Find each parasitized red blood cell.
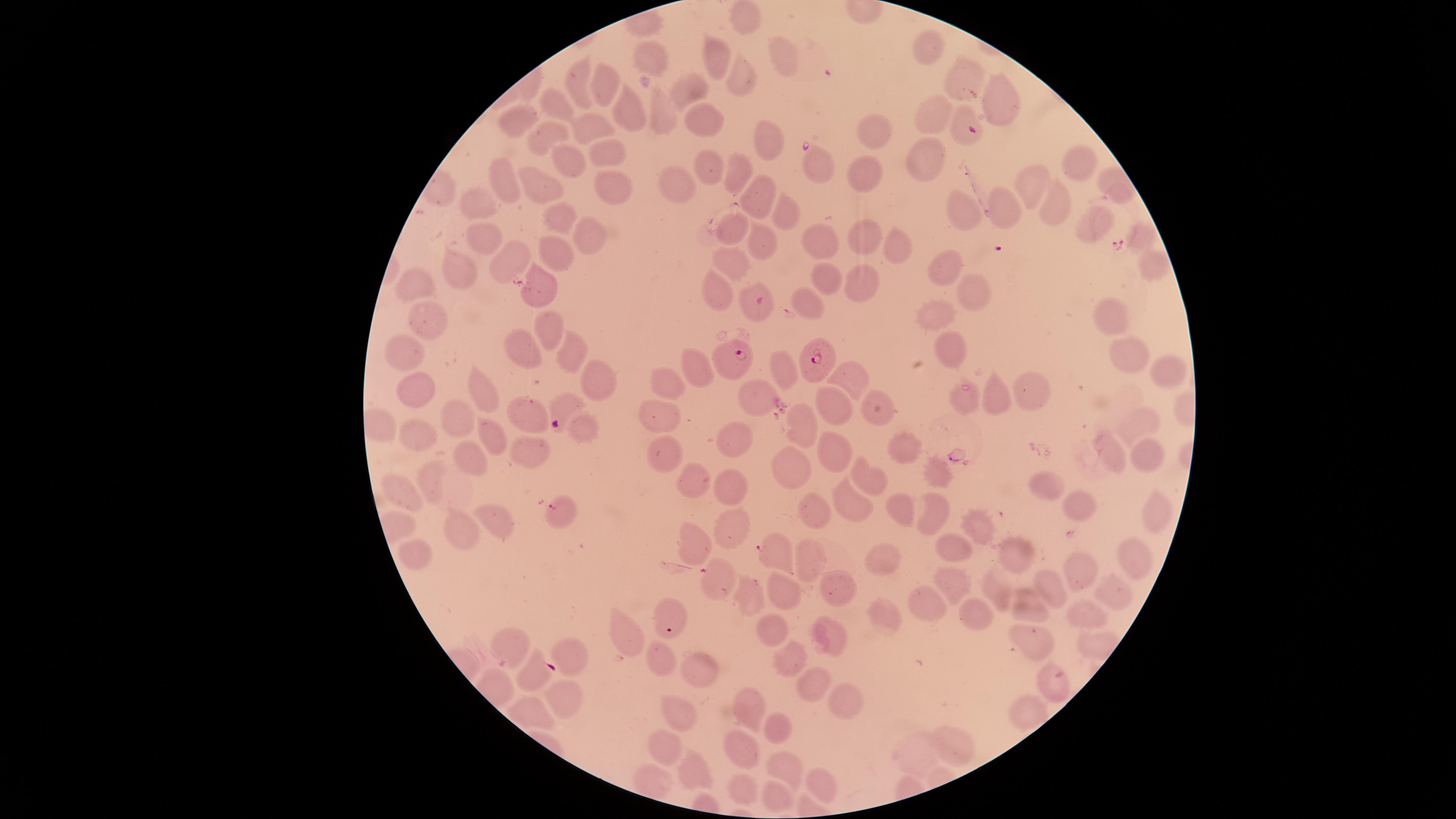
Approximate marker points as (x, y) in pixels.
Parasitized red blood cells: (974, 131), (739, 356), (815, 359), (559, 422), (770, 550), (710, 574), (535, 675).

Approximate marker points as (x, y) in pixels. Uninfected red blood cells: (744, 19), (719, 53), (930, 53), (779, 56), (651, 59), (579, 77), (742, 81), (963, 83), (604, 86), (685, 86), (993, 97), (553, 108), (632, 111), (660, 113), (936, 115), (517, 118), (708, 122), (593, 125), (873, 127), (545, 133), (762, 138), (606, 152), (922, 154), (1079, 160), (569, 161), (707, 167), (737, 168), (818, 168), (860, 168), (505, 175), (612, 181), (542, 184), (673, 184), (1033, 186), (753, 200), (479, 204), (1052, 210), (958, 211), (1006, 212), (551, 213), (783, 213), (1095, 220), (733, 227), (582, 229), (1140, 233), (483, 235), (863, 237), (757, 241), (818, 245), (895, 245), (553, 257), (507, 258), (731, 259), (1150, 261), (942, 267), (459, 269), (826, 279), (862, 280), (411, 284), (540, 288), (713, 288), (970, 296), (750, 302), (806, 305), (1115, 311), (939, 313), (426, 323), (542, 330), (529, 348), (403, 349), (952, 349), (568, 351), (1124, 352), (1165, 363), (700, 367), (783, 369), (852, 376), (595, 378), (666, 384), (1026, 388), (416, 390), (484, 394), (759, 396), (965, 396), (996, 396), (880, 406), (835, 409), (528, 411), (663, 417), (455, 422), (1139, 424), (801, 426), (582, 430), (418, 435), (489, 436), (734, 438), (901, 451), (1112, 451), (835, 454), (528, 455), (661, 455), (472, 457), (1148, 457), (787, 467), (939, 468), (862, 478), (430, 479), (693, 479), (728, 488), (1051, 488), (406, 495), (845, 503), (1078, 507), (1156, 509), (558, 510), (897, 510), (812, 511), (935, 518), (495, 520), (983, 525), (725, 528), (459, 533), (696, 539), (1023, 544), (955, 546), (417, 550), (1132, 554), (805, 555), (886, 557), (1078, 569), (951, 581), (999, 583), (780, 584), (833, 585), (1052, 589), (1117, 594), (748, 596), (1025, 604), (930, 605), (884, 609), (672, 613), (971, 613), (1086, 617), (770, 630), (830, 634), (1031, 636), (629, 637), (507, 642), (568, 654), (794, 654), (656, 657), (698, 666), (811, 685), (1053, 689), (845, 696), (562, 700), (750, 709), (677, 710), (780, 727), (956, 744), (667, 747), (742, 749), (910, 755), (783, 765), (694, 766), (821, 785), (738, 787), (776, 801). Thin blood smear. Image is 1456×819 pixels. Photographed with a smartphone camera through the microscope eyepiece. One field of view of the specimen. Giemsa stain. Species: Plasmodium falciparum. The visible region is circular.